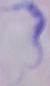

A trypanosome is seen. Captured at 1000x magnification. Photomicrograph.